Locate and identify every blood parasite.
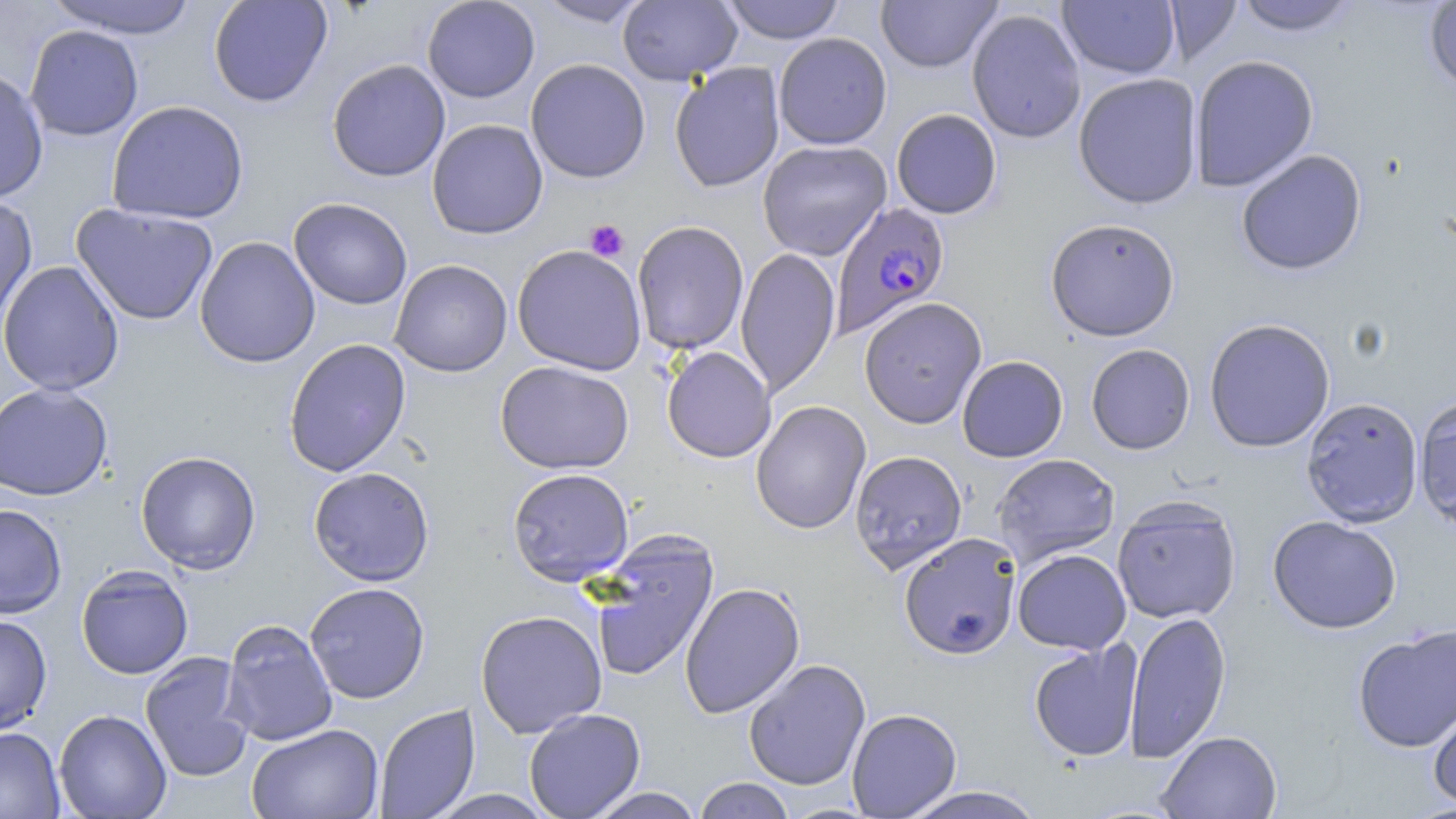
Approximate bounding boxes as (x1,y1)-(x2,y2) corner pairs in pixels.
Plasmodium falciparum-infected red blood cells: (831,201)-(950,338).
No Plasmodium ovale, Plasmodium malariae, Plasmodium vivax, Babesia divergens, or Trypanosoma brucei observed.

slide_level_diagnosis: Plasmodium falciparum
preparation: thin blood smear
modality: optical microscopy
magnification: 1000x
stain: May-Grünwald-Giemsa
platelet_locations: 'approximate bounding boxes as (x1,y1)-(x2,y2) corner pairs in pixels: (585,219)-(629,262)'
image_size: 1456×819 pixels
field_of_view: single
uninfected_red_blood_cell_locations: 'approximate bounding boxes as (x1,y1)-(x2,y2) corner pairs in pixels: (46,0)-(199,39), (208,0)-(332,108), (422,0)-(540,103), (534,0)-(653,27), (618,0)-(742,86), (722,0)-(845,44), (876,0)-(1002,73), (1164,0)-(1242,66), (1057,1)-(1180,79), (1233,1)-(1360,36), (1424,2)-(1456,93), (967,9)-(1086,144), (25,24)-(144,141), (773,32)-(892,150), (1189,55)-(1319,192), (525,58)-(651,183), (327,59)-(451,182), (670,62)-(785,192), (0,66)-(49,203), (1073,73)-(1203,209), (106,101)-(249,225), (891,109)-(1002,219), (427,119)-(547,239), (757,140)-(892,261), (1236,149)-(1367,275), (0,193)-(37,330), (289,197)-(412,310), (72,203)-(218,325), (1045,218)-(1180,341), (631,221)-(749,355), (194,236)-(320,368), (512,245)-(647,375), (735,247)-(840,398), (389,259)-(513,378), (0,260)-(125,396), (859,297)-(987,428), (1204,318)-(1335,453), (283,338)-(412,477), (1086,344)-(1195,455), (662,346)-(776,463), (957,355)-(1068,462), (495,360)-(633,474), (0,382)-(113,501), (1413,395)-(1456,530), (1300,396)-(1423,527), (751,400)-(871,534), (136,450)-(261,574), (849,450)-(967,573), (992,453)-(1121,565), (308,467)-(435,586), (507,467)-(634,586), (1111,497)-(1242,623), (0,503)-(67,618), (1267,516)-(1402,633), (587,529)-(720,684), (898,532)-(1021,660), (1012,549)-(1131,655), (76,564)-(193,680), (304,582)-(430,704), (680,582)-(805,718), (475,609)-(607,738), (1124,610)-(1231,763), (0,614)-(53,735), (220,619)-(338,746), (1353,625)-(1456,752), (1028,640)-(1144,762), (140,651)-(255,783), (743,658)-(871,790), (1428,694)-(1456,812), (374,703)-(480,819), (523,707)-(646,819), (847,708)-(962,818), (53,709)-(172,818), (246,724)-(383,819), (0,726)-(65,818), (1158,730)-(1282,818), (693,777)-(796,819), (899,786)-(1046,819), (586,787)-(704,819), (427,789)-(556,818)'